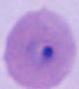

modality = photomicrograph
identification = Plasmodium
magnification = 400x or 1000x